Locate every Babesia divergens-infected red blood cell.
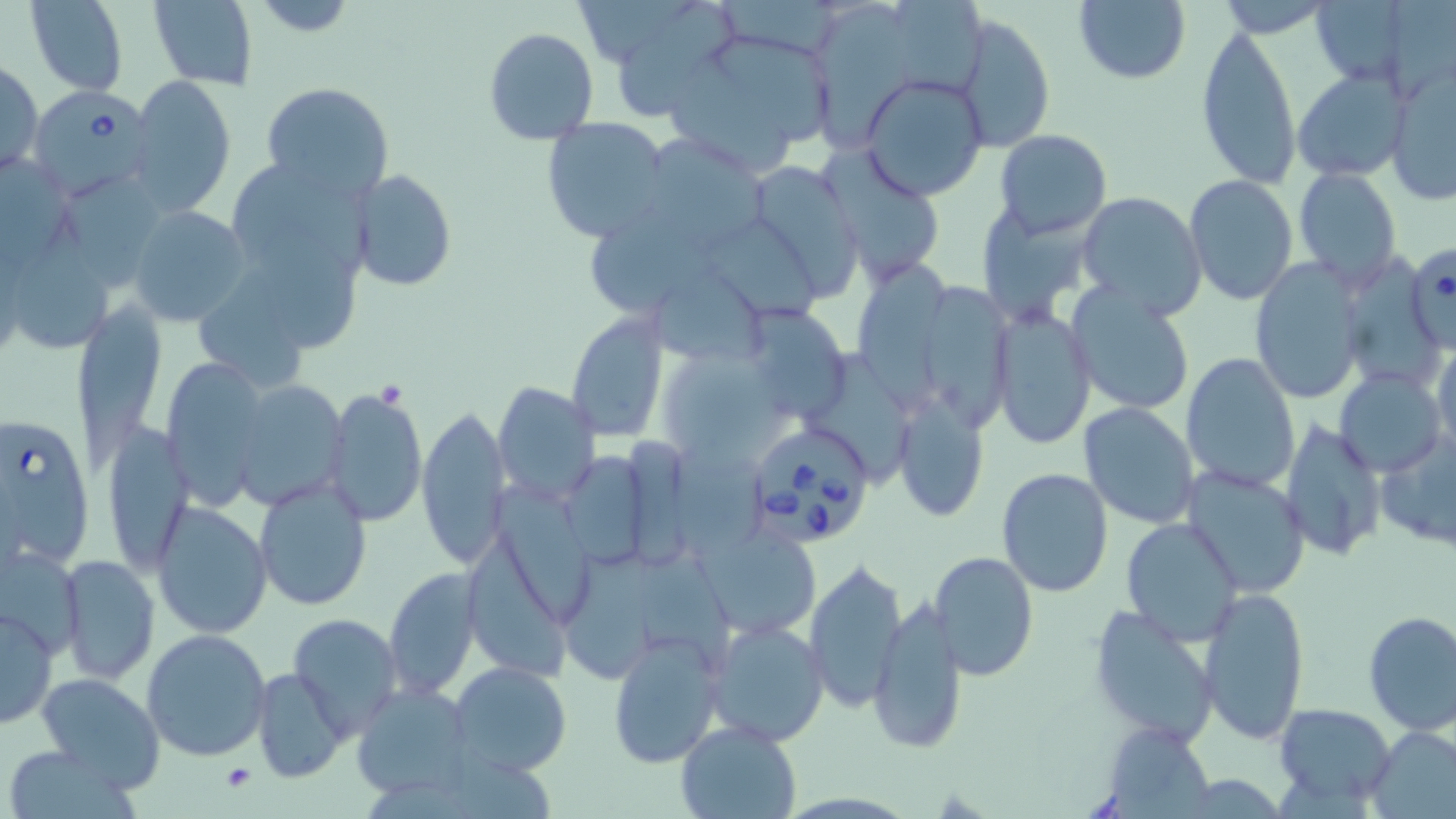
Approximate bounding boxes as [x1, y1, x2, y2] in pixels.
Babesia divergens-infected red blood cells: [29, 84, 158, 204], [1406, 240, 1454, 357], [0, 411, 95, 574], [743, 420, 878, 549].

slide-level diagnosis = Babesia divergens
stain = May-Grünwald-Giemsa
field of view = one of a larger specimen
magnification = 1000x
image size = 1456×819 pixels
uninfected red blood cell locations = approximate bounding boxes as [x1, y1, x2, y2] in pixels: [26, 0, 129, 95], [723, 0, 858, 61], [1074, 0, 1191, 85], [147, 1, 258, 88], [243, 1, 364, 36], [895, 1, 987, 94], [1305, 1, 1427, 88], [616, 2, 736, 124], [817, 3, 915, 152], [956, 14, 1056, 155], [1195, 25, 1301, 188], [483, 28, 599, 146], [663, 33, 834, 173], [1, 57, 43, 180], [1386, 66, 1456, 203], [1292, 70, 1411, 182], [130, 74, 236, 218], [862, 74, 988, 200], [261, 82, 395, 202], [541, 118, 670, 243], [993, 130, 1112, 240], [653, 138, 767, 249], [821, 145, 940, 281], [1, 153, 67, 280], [229, 159, 381, 274], [741, 161, 866, 303], [1293, 166, 1402, 290], [351, 168, 458, 291], [1185, 174, 1299, 305], [68, 180, 164, 285], [1076, 191, 1208, 318], [974, 200, 1092, 330], [128, 205, 252, 327], [16, 219, 115, 344], [594, 222, 728, 316], [264, 230, 358, 350], [851, 257, 954, 419], [1250, 258, 1367, 405], [200, 267, 312, 390], [656, 275, 763, 357], [926, 278, 1015, 431], [1064, 284, 1195, 417], [748, 298, 845, 418], [76, 299, 159, 469], [991, 308, 1097, 449], [565, 314, 670, 444], [1431, 335, 1456, 462], [666, 344, 774, 444], [1181, 352, 1301, 495], [815, 354, 916, 479], [158, 357, 270, 509], [1338, 366, 1445, 480], [229, 379, 351, 511], [493, 380, 599, 504], [322, 388, 425, 528], [890, 395, 989, 524], [1077, 403, 1200, 530], [416, 406, 510, 571], [101, 420, 195, 574], [1280, 420, 1388, 560], [1376, 426, 1456, 554], [678, 445, 774, 554], [555, 451, 658, 570], [1180, 465, 1311, 599], [995, 467, 1112, 598], [254, 479, 374, 612], [492, 485, 593, 626], [151, 502, 274, 639], [1119, 516, 1243, 646], [696, 526, 819, 639], [0, 544, 86, 660], [467, 544, 568, 677], [560, 546, 666, 681], [934, 551, 1039, 683], [58, 553, 161, 687], [635, 555, 744, 673], [805, 561, 908, 712], [383, 567, 481, 701], [1199, 586, 1310, 743], [868, 597, 968, 756], [1087, 604, 1221, 746], [0, 605, 57, 730], [1361, 610, 1456, 736], [287, 613, 404, 738], [704, 618, 828, 747], [141, 629, 274, 762], [608, 631, 724, 770], [448, 661, 573, 776], [250, 667, 352, 782], [36, 673, 167, 791], [353, 682, 475, 803], [1273, 703, 1396, 804], [675, 721, 802, 818], [1099, 723, 1213, 815], [1367, 726, 1456, 819], [3, 744, 138, 818]
platelet locations = approximate bounding boxes as [x1, y1, x2, y2] in pixels: [221, 763, 257, 792]
preparation = thin blood smear
modality = optical microscopy